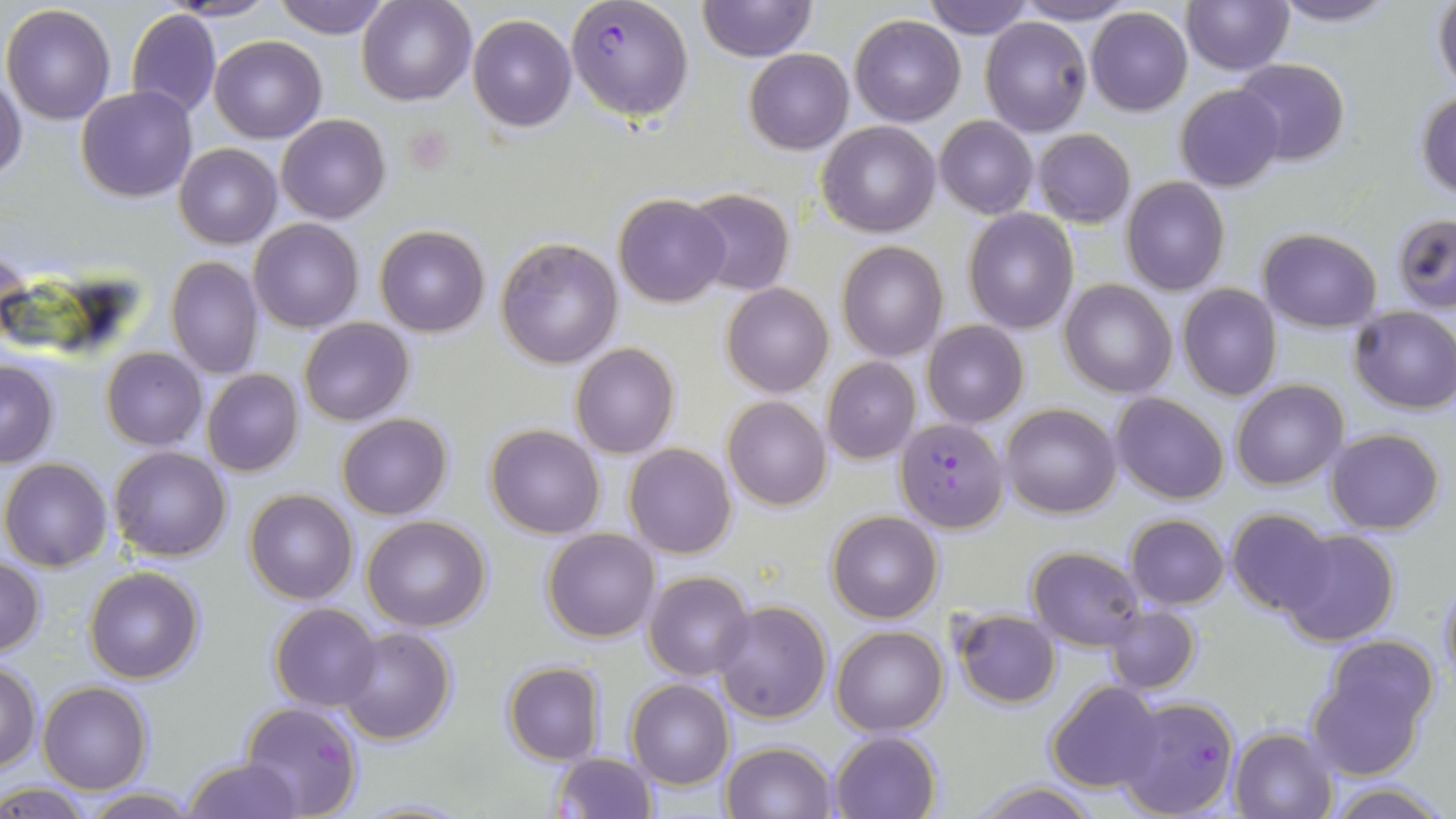 Approximate bounding boxes as (x1, y1, x2, y2) in pixels. Plasmodium falciparum-infected red blood cell locations: (566, 0, 693, 120), (895, 417, 1006, 532), (1118, 696, 1240, 819). Uninfected red blood cell locations: (273, 0, 392, 39), (357, 0, 475, 105), (697, 0, 818, 64), (921, 0, 1034, 39), (1181, 0, 1294, 75), (1269, 0, 1399, 26), (1432, 0, 1456, 97), (167, 1, 280, 22), (1013, 1, 1138, 25), (2, 4, 117, 126), (1086, 7, 1192, 115), (126, 9, 220, 120), (468, 13, 576, 131), (849, 14, 965, 125), (980, 17, 1092, 136), (209, 34, 326, 142), (745, 49, 853, 154), (1232, 58, 1351, 166), (0, 75, 27, 184), (1175, 84, 1286, 192), (75, 85, 197, 203), (1415, 89, 1456, 200), (277, 115, 390, 223), (935, 116, 1038, 219), (818, 120, 941, 237), (1033, 129, 1135, 227), (173, 141, 282, 249), (1121, 176, 1229, 295), (684, 190, 794, 295), (613, 193, 731, 307), (964, 208, 1077, 332), (1393, 213, 1456, 312), (249, 218, 363, 332), (375, 225, 490, 337), (1257, 228, 1382, 330), (495, 238, 622, 368), (837, 241, 947, 361), (166, 256, 264, 379), (1061, 280, 1177, 399), (722, 283, 834, 398), (1177, 284, 1282, 401), (1348, 306, 1456, 414), (299, 317, 414, 425), (922, 321, 1029, 428), (570, 343, 680, 459), (101, 347, 206, 450), (822, 357, 920, 464), (0, 358, 59, 468), (202, 369, 304, 477), (1231, 380, 1347, 489), (1109, 392, 1230, 505), (723, 396, 832, 510), (1002, 403, 1120, 518), (337, 413, 453, 520), (485, 424, 607, 538), (1325, 428, 1445, 534), (624, 443, 736, 560), (109, 446, 232, 562), (1, 458, 114, 571), (244, 489, 358, 604), (1227, 507, 1340, 615), (826, 510, 942, 624), (1126, 514, 1229, 608), (361, 515, 492, 632), (1276, 527, 1401, 647), (542, 529, 661, 643), (1027, 547, 1144, 650), (0, 557, 47, 656), (84, 566, 204, 683), (645, 570, 755, 680), (1437, 577, 1456, 687), (713, 599, 833, 723), (269, 604, 381, 712), (1105, 605, 1200, 694), (952, 609, 1060, 708), (830, 624, 948, 735), (335, 626, 457, 745), (1321, 634, 1439, 735), (1, 662, 42, 771), (502, 662, 606, 765), (1307, 667, 1425, 780), (626, 678, 734, 789), (38, 681, 153, 794), (1046, 681, 1164, 793), (241, 700, 362, 819), (1229, 727, 1337, 818), (830, 730, 942, 819), (719, 742, 835, 819), (552, 752, 656, 819), (183, 757, 302, 817), (970, 780, 1098, 819), (1326, 782, 1450, 818), (0, 785, 97, 818), (79, 789, 202, 818). Platelet locations: (404, 124, 454, 174). Slide-level diagnosis: Plasmodium falciparum. Optical microscopy. Single field of view. Captured at 1000x magnification. Image is 1456×819 pixels. May-Grünwald-Giemsa-stained preparation. Thin blood film.